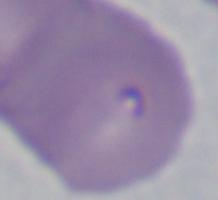

magnification: 1000x
identification: Babesia
modality: photomicrograph